Outline each blood parasite and name the species.
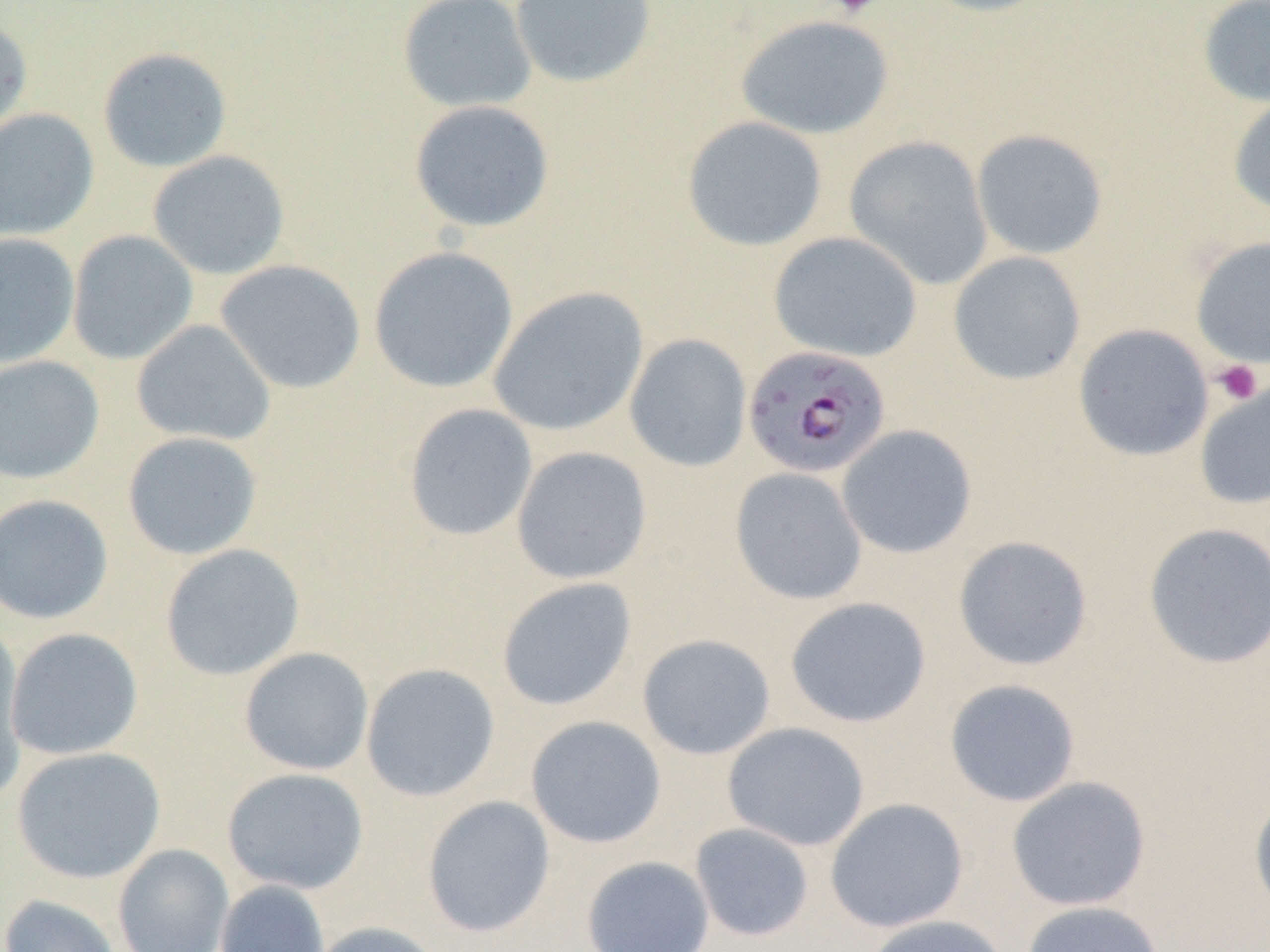
Approximate bounding boxes as named x1/y1/x2/y2 corners in pixels.
Plasmodium falciparum-infected red blood cells: (x1=742, y1=345, x2=892, y2=479).
No Plasmodium ovale, Plasmodium malariae, Plasmodium vivax, Babesia divergens, or Trypanosoma brucei observed.

{
  "slide_level_diagnosis": "Plasmodium falciparum",
  "field_of_view": "one of a larger specimen",
  "image_size": "1270×952 pixels",
  "modality": "light microscopy",
  "platelet_locations": "approximate bounding boxes as named x1/y1/x2/y2 corners in pixels: (x1=828, y1=0, x2=883, y2=18), (x1=1212, y1=359, x2=1263, y2=406)",
  "uninfected_red_blood_cell_locations": "approximate bounding boxes as named x1/y1/x2/y2 corners in pixels: (x1=397, y1=0, x2=537, y2=113), (x1=510, y1=0, x2=658, y2=88), (x1=915, y1=0, x2=1058, y2=18), (x1=1197, y1=0, x2=1270, y2=108), (x1=733, y1=13, x2=896, y2=140), (x1=0, y1=17, x2=33, y2=146), (x1=97, y1=46, x2=232, y2=173), (x1=1227, y1=94, x2=1270, y2=219), (x1=408, y1=100, x2=555, y2=233), (x1=0, y1=108, x2=100, y2=241), (x1=682, y1=116, x2=828, y2=252), (x1=970, y1=128, x2=1109, y2=260), (x1=843, y1=135, x2=994, y2=290), (x1=147, y1=150, x2=290, y2=280), (x1=66, y1=230, x2=198, y2=365), (x1=768, y1=231, x2=922, y2=362), (x1=0, y1=233, x2=80, y2=368), (x1=1190, y1=235, x2=1270, y2=370), (x1=368, y1=246, x2=518, y2=394), (x1=947, y1=251, x2=1086, y2=386), (x1=214, y1=259, x2=366, y2=394), (x1=488, y1=286, x2=648, y2=437), (x1=131, y1=319, x2=276, y2=447), (x1=1073, y1=324, x2=1214, y2=461), (x1=624, y1=333, x2=752, y2=472), (x1=0, y1=355, x2=105, y2=485), (x1=1194, y1=379, x2=1270, y2=510), (x1=403, y1=403, x2=538, y2=541), (x1=836, y1=424, x2=977, y2=559), (x1=122, y1=431, x2=263, y2=560), (x1=511, y1=446, x2=653, y2=585), (x1=729, y1=466, x2=868, y2=605), (x1=0, y1=493, x2=114, y2=625), (x1=1142, y1=522, x2=1270, y2=669), (x1=953, y1=535, x2=1093, y2=671), (x1=159, y1=544, x2=305, y2=681), (x1=496, y1=577, x2=638, y2=712), (x1=785, y1=596, x2=931, y2=728), (x1=0, y1=624, x2=30, y2=806), (x1=5, y1=627, x2=143, y2=761), (x1=637, y1=633, x2=776, y2=760), (x1=238, y1=647, x2=374, y2=776), (x1=360, y1=663, x2=500, y2=802), (x1=944, y1=678, x2=1082, y2=807), (x1=525, y1=715, x2=667, y2=848), (x1=722, y1=721, x2=870, y2=851), (x1=11, y1=746, x2=166, y2=884), (x1=221, y1=767, x2=369, y2=894), (x1=1006, y1=776, x2=1151, y2=911), (x1=1249, y1=789, x2=1270, y2=918), (x1=421, y1=795, x2=556, y2=937), (x1=824, y1=798, x2=969, y2=933), (x1=689, y1=822, x2=815, y2=941), (x1=112, y1=844, x2=234, y2=952), (x1=581, y1=855, x2=715, y2=951), (x1=214, y1=880, x2=330, y2=952), (x1=0, y1=894, x2=123, y2=952), (x1=1020, y1=900, x2=1167, y2=952), (x1=862, y1=914, x2=1011, y2=952), (x1=308, y1=920, x2=449, y2=952)",
  "magnification": "1000x",
  "preparation": "thin blood smear"
}